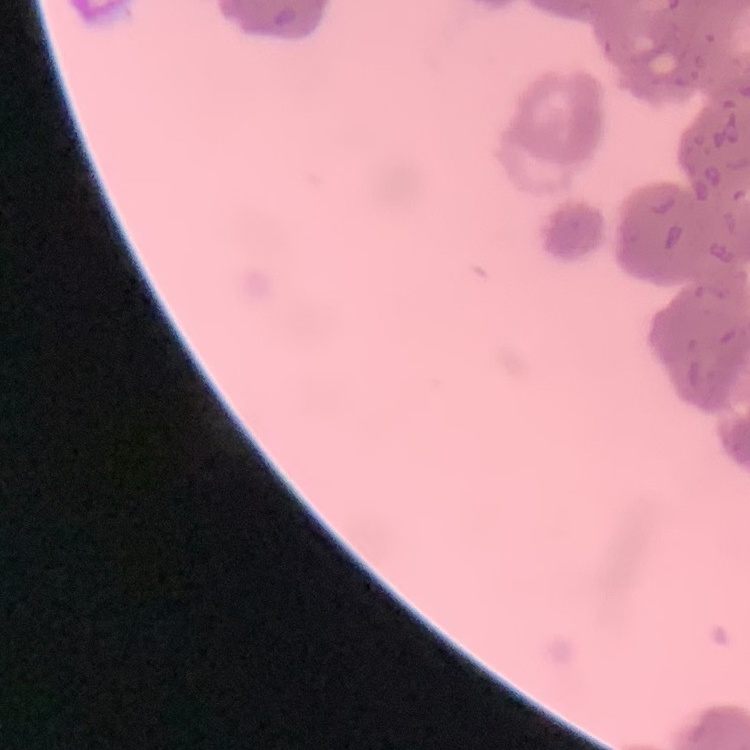
Summary:
  - Red blood cell morphology: rouleaux formation
  - Preparation: thin peripheral smear
  - Image type: one tile cut from a larger photomicrograph
  - Stain: Field's or Giemsa